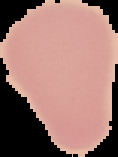

{
  "image_size": "118×157 pixels",
  "image_type": "cell region segmented out of the field of view; surrounding area masked to black",
  "result": "no Plasmodium parasites seen",
  "preparation": "thin blood smear"
}